Give the preparation type.
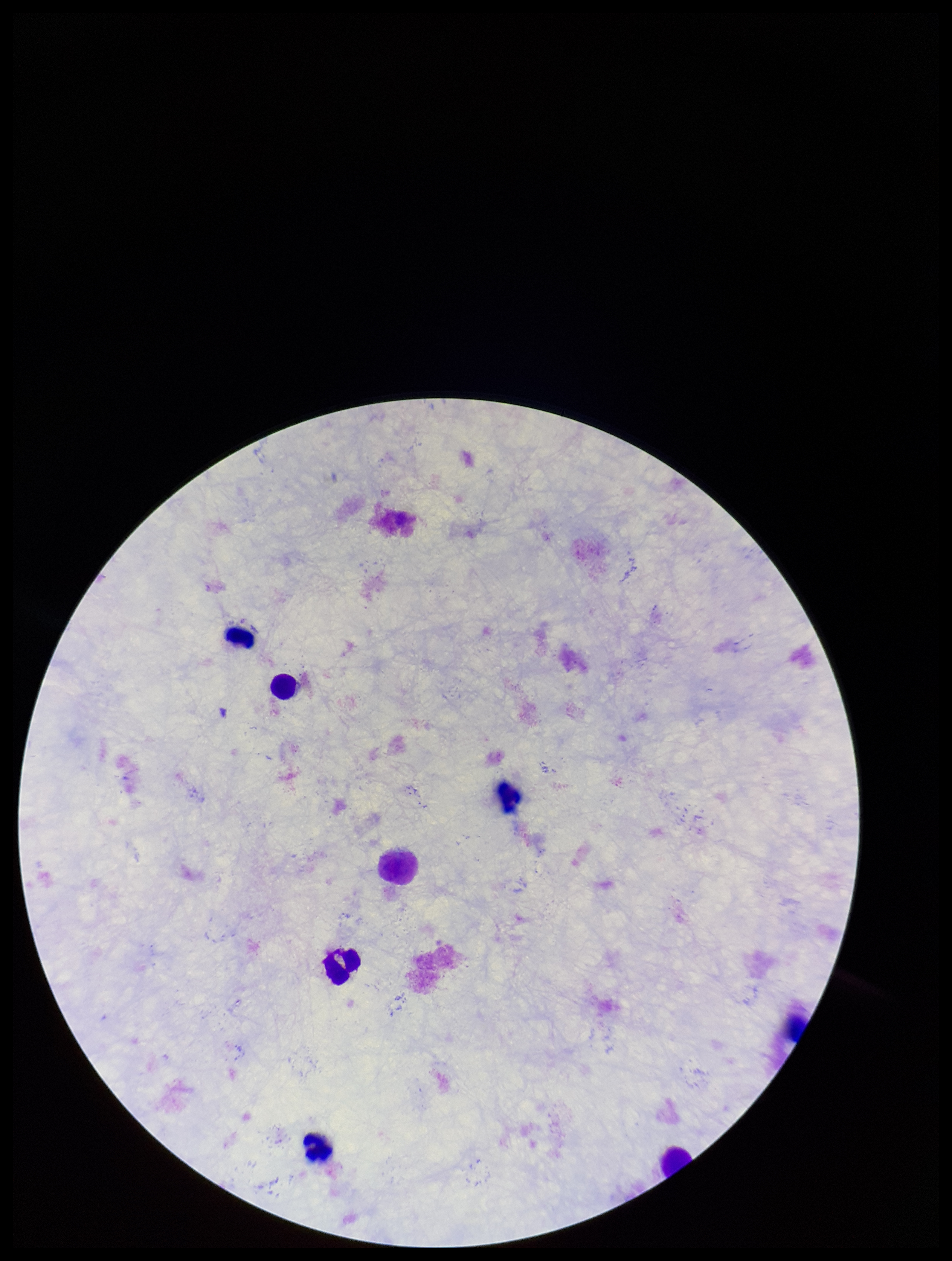

Thick.

image size = 952×1261 pixels
Plasmodium parasites = none seen
capture = smartphone photograph through the microscope eyepiece
patient malaria status = negative
field of view = single
leukocyte count = 7
parasite count = 0
stain = Giemsa